Describe the morphology of the red blood cells.
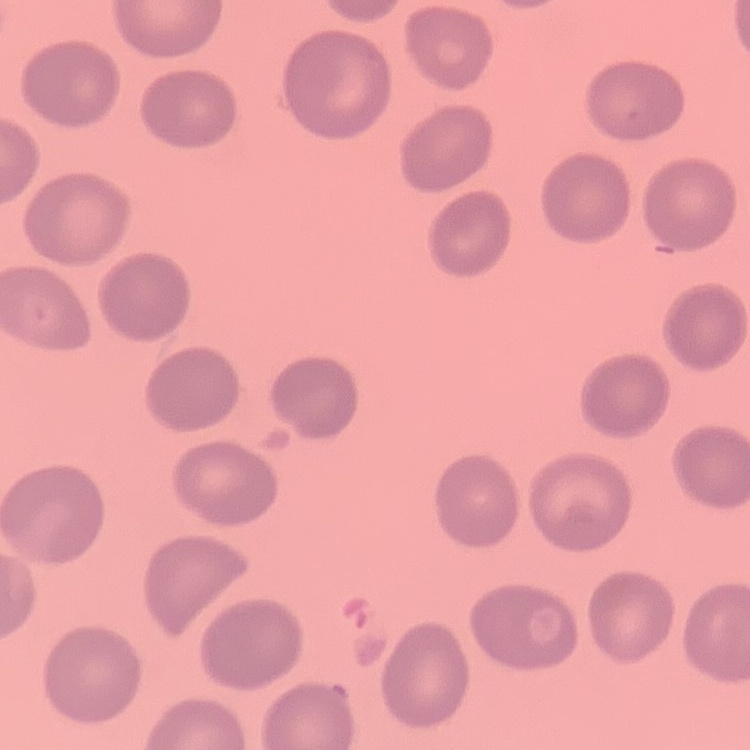

No rouleaux formation.

Summary:
  - Preparation: thin blood smear
  - Image type: square crop of a larger photomicrograph
  - Stain: Field's or Giemsa